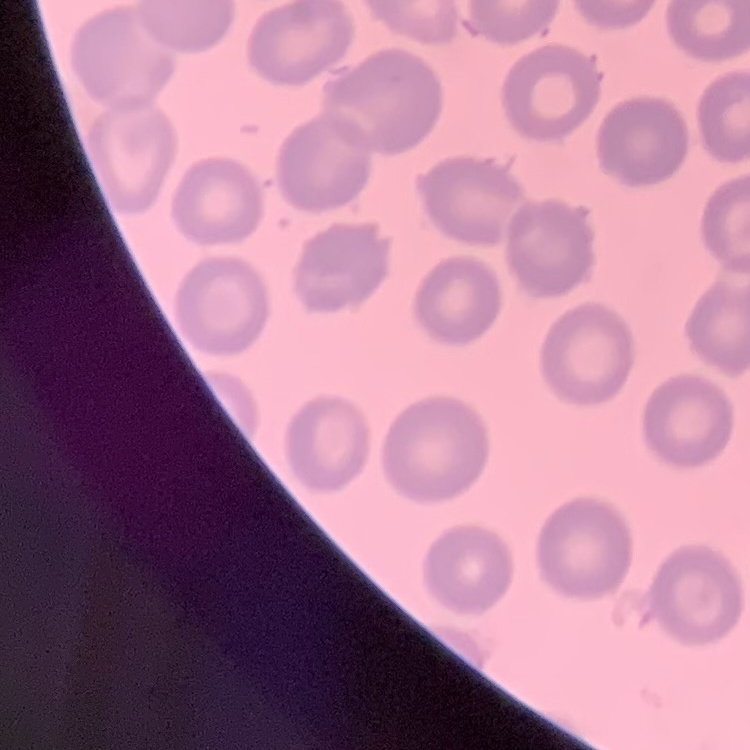

{
  "erythrocyte_morphology": "no rouleaux formation",
  "image_type": "one tile cut from a larger photomicrograph",
  "preparation": "thin peripheral smear",
  "stain": "Field's or Giemsa"
}